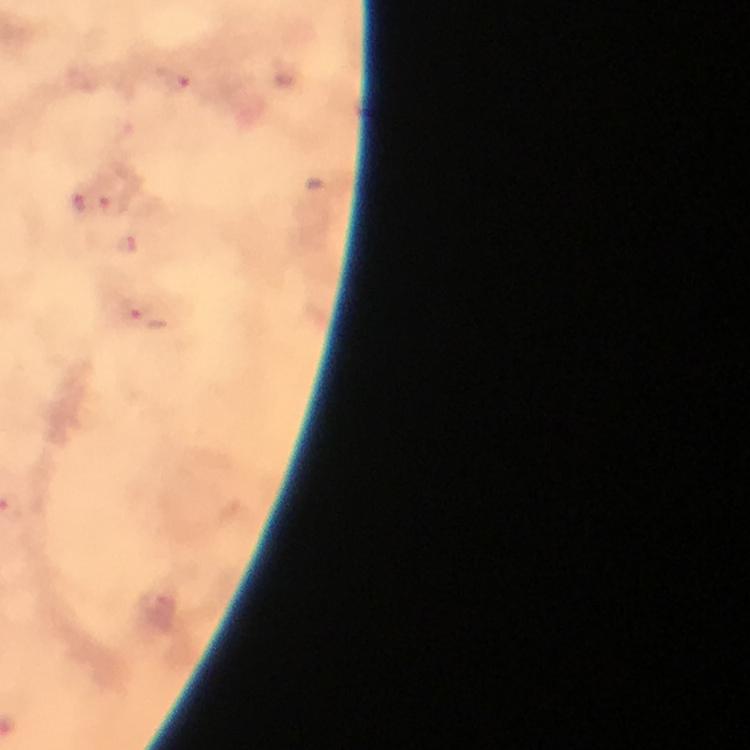
Approximate centers as (x, y) in pixels.
Summary:
  - Plasmodium parasite locations: (173, 79), (80, 202), (115, 206), (128, 245), (136, 308)
  - Immersion oil: used
  - Image size: 750×750 pixels
  - Context: from a diagnostic examination for malaria
  - Magnification: 100x
  - Stain: Giemsa
  - Preparation: thick blood film
  - Capture: smartphone mounted on the microscope
  - Cropped from: one field of view